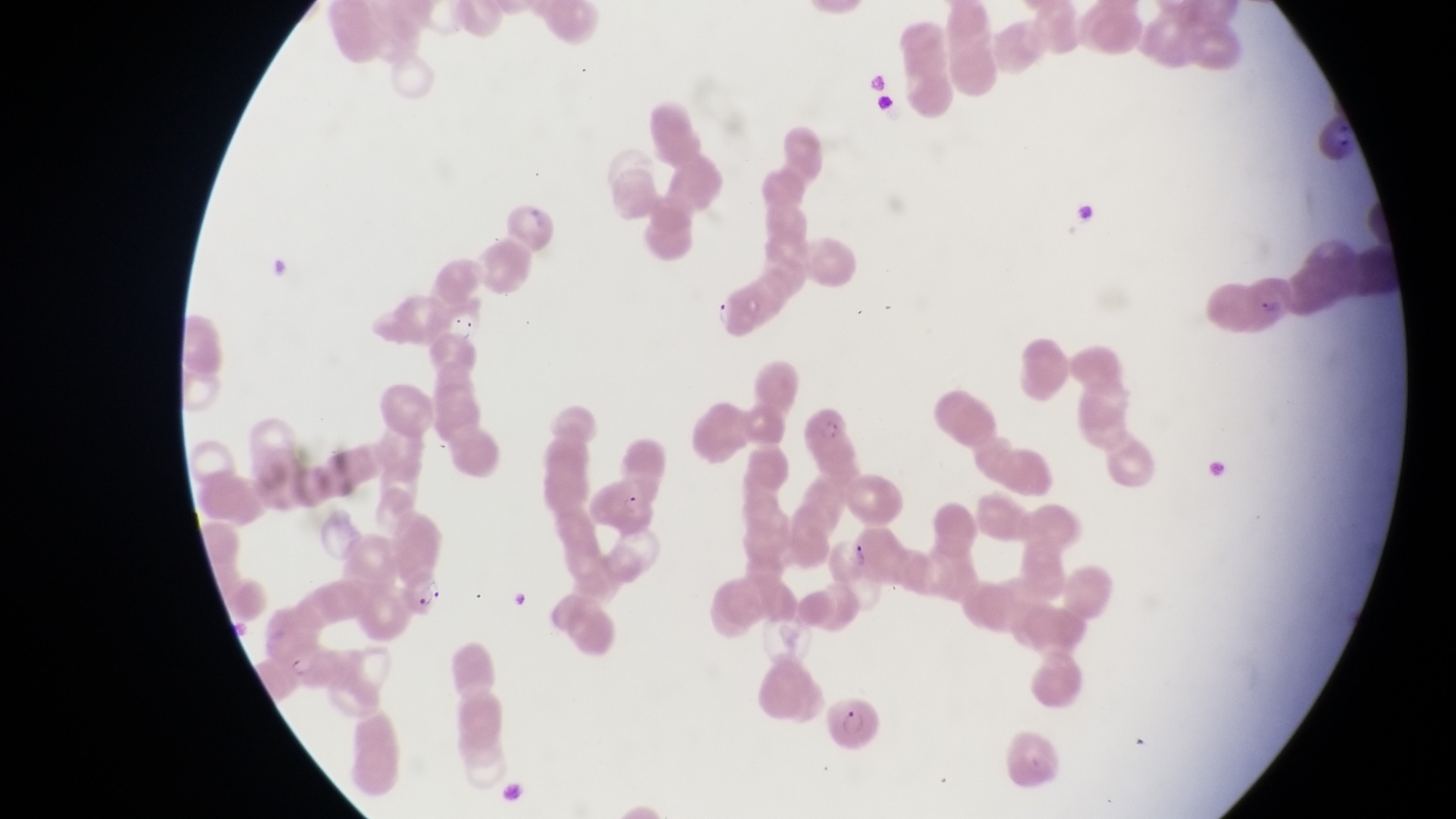
capture: smartphone photograph through the eyepiece of an Olympus CX-23 microscope
field_of_view: single
parasitised_red_blood_cell_locations: 'approximate bounding boxes as (left, top, right, bottom) in pixels: (1247, 274, 1292, 335), (585, 472, 662, 531), (829, 534, 878, 593), (400, 576, 450, 622), (824, 695, 888, 755)'
trophozoite_locations: 'approximate bounding boxes as (left, top, right, bottom) in pixels: (704, 293, 738, 330), (438, 304, 485, 347)'
country: Uganda
image_size: 1456×819 pixels
magnification: 1000x
preparation: thin blood smear